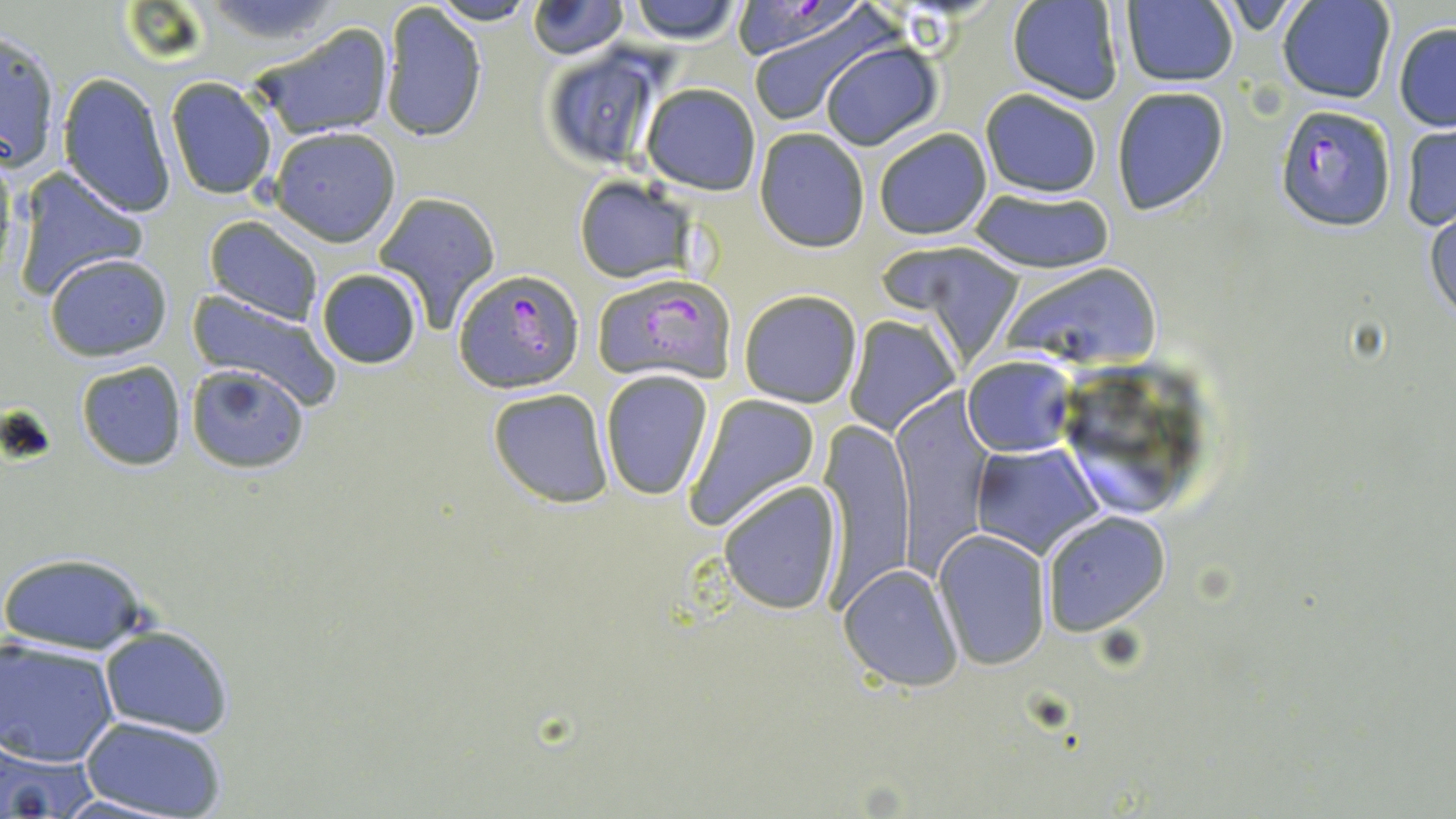

Summary:
  - Coordinate format: approximate bounding boxes as (x1,y1)-(x2,y2) corner pairs in pixels
  - Plasmodium falciparum-infected red blood cell locations: (1275,104)-(1397,232), (454,268)-(585,392), (593,274)-(738,384)
  - Uninfected red blood cell locations: (528,0)-(628,58), (626,0)-(743,44), (432,1)-(534,26), (1006,1)-(1124,105), (1276,1)-(1396,105), (1119,2)-(1239,87), (379,3)-(489,144), (742,14)-(885,125), (246,22)-(395,141), (1393,23)-(1456,132), (1,27)-(63,174), (819,40)-(943,151), (538,44)-(665,169), (190,46)-(367,179), (58,73)-(177,219), (164,77)-(278,201), (640,83)-(760,195), (1110,86)-(1230,216), (978,88)-(1103,197), (1401,123)-(1456,232), (268,126)-(403,246), (754,128)-(870,252), (872,129)-(992,240), (13,166)-(149,301), (573,176)-(694,283), (971,188)-(1115,271), (372,191)-(501,329), (1426,209)-(1456,326), (203,215)-(323,325), (898,243)-(1028,367), (44,252)-(174,362), (999,262)-(1161,368), (315,268)-(422,369), (738,289)-(862,408), (183,292)-(343,413), (845,314)-(959,436), (962,354)-(1074,456), (76,360)-(187,470), (185,363)-(310,473), (600,369)-(713,501), (486,386)-(615,507), (683,395)-(821,531), (890,398)-(995,580), (817,422)-(917,607), (970,443)-(1103,558), (717,480)-(842,614), (1040,511)-(1170,637), (933,528)-(1051,668), (0,551)-(150,655), (839,563)-(965,691), (100,627)-(234,739), (1,638)-(120,766), (80,716)-(229,818), (0,739)-(96,817), (49,793)-(193,818)
  - Slide-level diagnosis: Plasmodium falciparum
  - Magnification: 1000x
  - Image size: 1456×819 pixels
  - Preparation: thin blood smear
  - Field of view: one of a larger specimen
  - Modality: light microscopy
  - Stain: May-Grünwald-Giemsa